Identify the parasite.
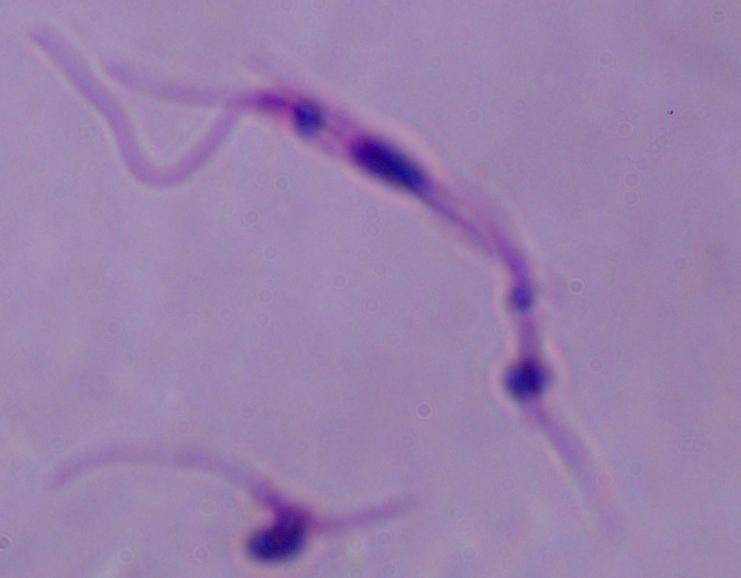
This is Leishmania.

Captured at 1000x magnification. Photomicrograph.